State the blood parasite species.
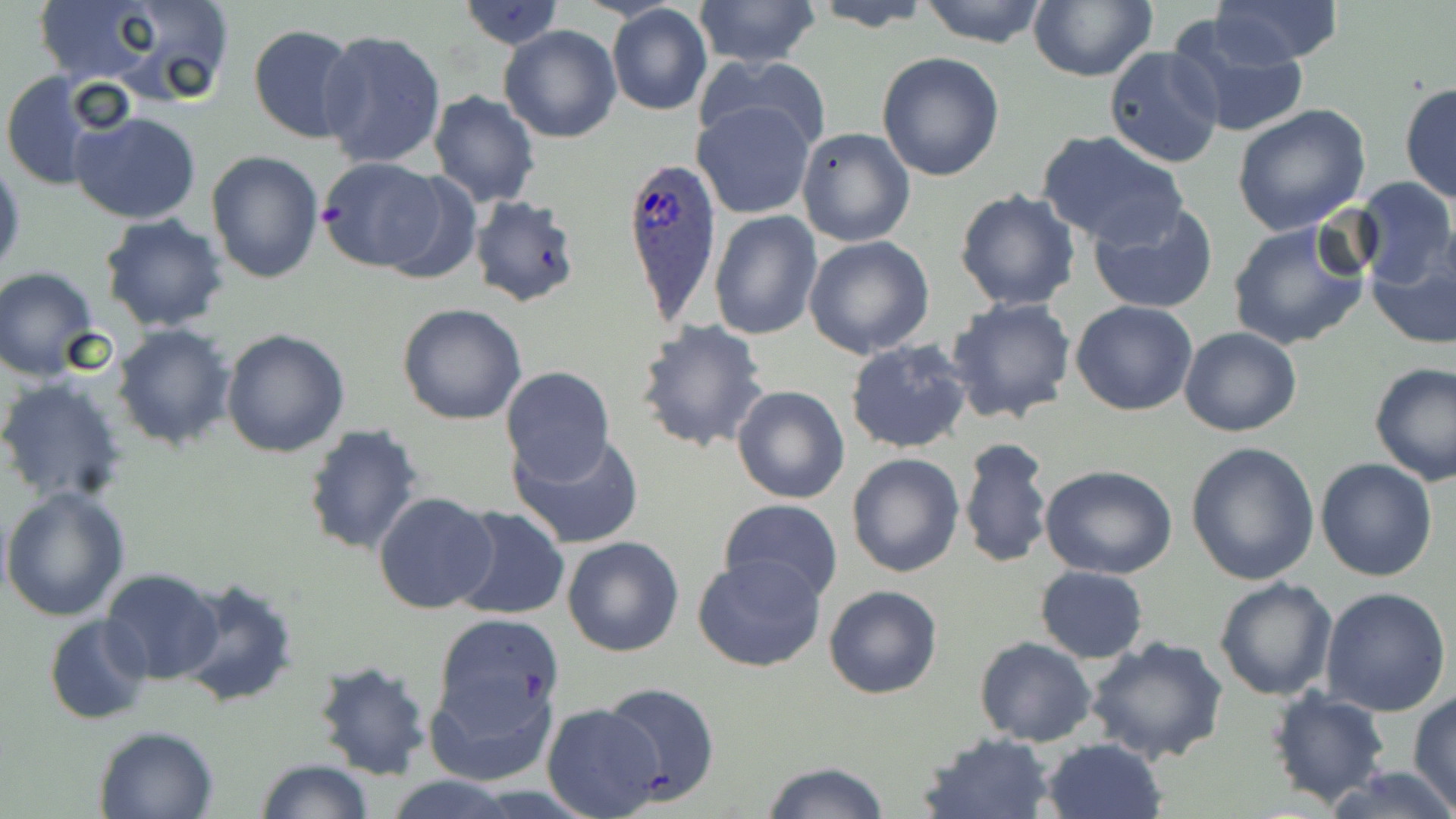

Plasmodium ovale.

uninfected red blood cell locations = approximate bounding boxes as named x1/y1/x2/y2 corners in pixels: (x1=26, y1=0, x2=179, y2=89), (x1=88, y1=0, x2=236, y2=105), (x1=691, y1=0, x2=821, y2=70), (x1=918, y1=0, x2=1049, y2=47), (x1=1210, y1=0, x2=1342, y2=65), (x1=459, y1=1, x2=563, y2=50), (x1=804, y1=1, x2=936, y2=32), (x1=1028, y1=1, x2=1156, y2=82), (x1=606, y1=5, x2=713, y2=117), (x1=1167, y1=13, x2=1309, y2=141), (x1=248, y1=24, x2=360, y2=143), (x1=499, y1=24, x2=622, y2=143), (x1=317, y1=28, x2=447, y2=170), (x1=1103, y1=46, x2=1224, y2=170), (x1=876, y1=52, x2=1005, y2=181), (x1=695, y1=53, x2=833, y2=158), (x1=0, y1=72, x2=105, y2=192), (x1=1399, y1=81, x2=1456, y2=205), (x1=428, y1=91, x2=541, y2=207), (x1=693, y1=99, x2=816, y2=218), (x1=1231, y1=103, x2=1371, y2=235), (x1=71, y1=109, x2=202, y2=225), (x1=796, y1=127, x2=916, y2=248), (x1=1036, y1=130, x2=1188, y2=248), (x1=206, y1=149, x2=324, y2=284), (x1=0, y1=156, x2=25, y2=280), (x1=315, y1=157, x2=453, y2=273), (x1=1351, y1=176, x2=1455, y2=287), (x1=954, y1=188, x2=1081, y2=311), (x1=468, y1=194, x2=584, y2=309), (x1=1086, y1=199, x2=1219, y2=315), (x1=710, y1=210, x2=823, y2=340), (x1=99, y1=214, x2=230, y2=332), (x1=1226, y1=218, x2=1372, y2=350), (x1=803, y1=235, x2=934, y2=359), (x1=1366, y1=246, x2=1456, y2=349), (x1=1, y1=268, x2=100, y2=380), (x1=946, y1=297, x2=1077, y2=424), (x1=1071, y1=301, x2=1198, y2=416), (x1=396, y1=302, x2=528, y2=426), (x1=635, y1=318, x2=770, y2=454), (x1=112, y1=323, x2=237, y2=450), (x1=1179, y1=327, x2=1302, y2=437), (x1=221, y1=329, x2=350, y2=459), (x1=844, y1=337, x2=974, y2=455), (x1=1369, y1=360, x2=1456, y2=485), (x1=498, y1=365, x2=615, y2=486), (x1=1, y1=376, x2=129, y2=506), (x1=732, y1=384, x2=850, y2=505), (x1=302, y1=424, x2=424, y2=558), (x1=508, y1=431, x2=646, y2=550), (x1=958, y1=437, x2=1053, y2=570), (x1=1186, y1=441, x2=1320, y2=584), (x1=846, y1=452, x2=964, y2=577), (x1=1315, y1=458, x2=1438, y2=582), (x1=1039, y1=463, x2=1178, y2=579), (x1=1, y1=486, x2=130, y2=621), (x1=372, y1=489, x2=497, y2=615), (x1=719, y1=499, x2=843, y2=603), (x1=448, y1=506, x2=570, y2=621), (x1=562, y1=535, x2=685, y2=658), (x1=692, y1=554, x2=826, y2=673), (x1=1034, y1=565, x2=1148, y2=663), (x1=100, y1=568, x2=226, y2=685), (x1=174, y1=575, x2=299, y2=709), (x1=1213, y1=577, x2=1338, y2=700), (x1=823, y1=585, x2=943, y2=699), (x1=1320, y1=587, x2=1452, y2=717), (x1=43, y1=614, x2=153, y2=726), (x1=432, y1=614, x2=564, y2=747), (x1=1082, y1=635, x2=1229, y2=764), (x1=975, y1=637, x2=1096, y2=747), (x1=311, y1=658, x2=435, y2=782), (x1=423, y1=666, x2=558, y2=788), (x1=600, y1=681, x2=720, y2=804), (x1=1267, y1=687, x2=1391, y2=807), (x1=1408, y1=693, x2=1456, y2=810), (x1=540, y1=703, x2=664, y2=817), (x1=93, y1=724, x2=220, y2=818), (x1=917, y1=732, x2=1056, y2=818), (x1=1040, y1=737, x2=1165, y2=819), (x1=254, y1=759, x2=373, y2=818), (x1=759, y1=761, x2=891, y2=818), (x1=1325, y1=764, x2=1456, y2=819), (x1=383, y1=775, x2=522, y2=818)
modality = optical microscopy
Plasmodium ovale-infected red blood cell locations = approximate bounding boxes as named x1/y1/x2/y2 corners in pixels: (x1=619, y1=153, x2=720, y2=325)
preparation = thin blood film
image size = 1456×819 pixels
field of view = one of a larger specimen
magnification = 1000x
stain = May-Grünwald-Giemsa